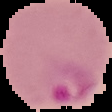
Image is 112×112 pixels. Result: Plasmodium parasites identified. Segmented cell region on a black background. From a thin blood smear.